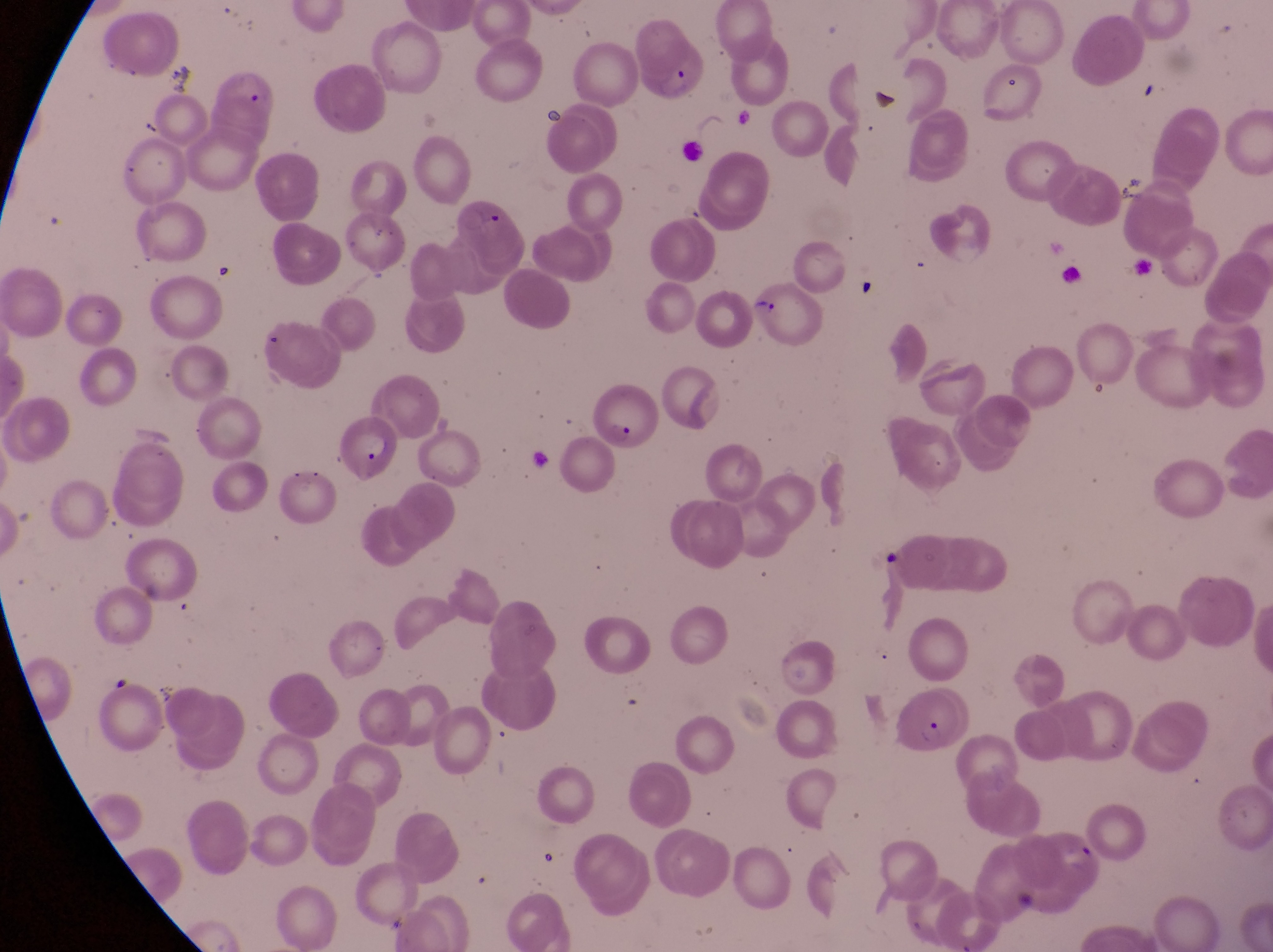
Approximate bounding boxes as (left, top, right, bottom) in pixels.
Summary:
  - Parasitised red blood cell locations: (639, 47, 709, 102), (212, 63, 277, 123), (535, 100, 570, 128), (749, 282, 829, 350), (591, 385, 663, 453), (337, 422, 395, 480), (894, 686, 957, 760), (1038, 817, 1108, 902)
  - Artifact (platelet-like body, stain precipitate, or debris) locations: (162, 58, 192, 91), (873, 87, 898, 109), (1109, 170, 1152, 205), (475, 204, 500, 229), (856, 270, 891, 317), (881, 545, 909, 580)
  - Image size: 1273×952 pixels
  - Capture: smartphone photograph through the eyepiece of an Olympus CX-23 microscope
  - Magnification: 1000x
  - Country: Uganda
  - Field of view: single
  - Preparation: thin blood film